Outline Plasmodium parasites and white blood cells.
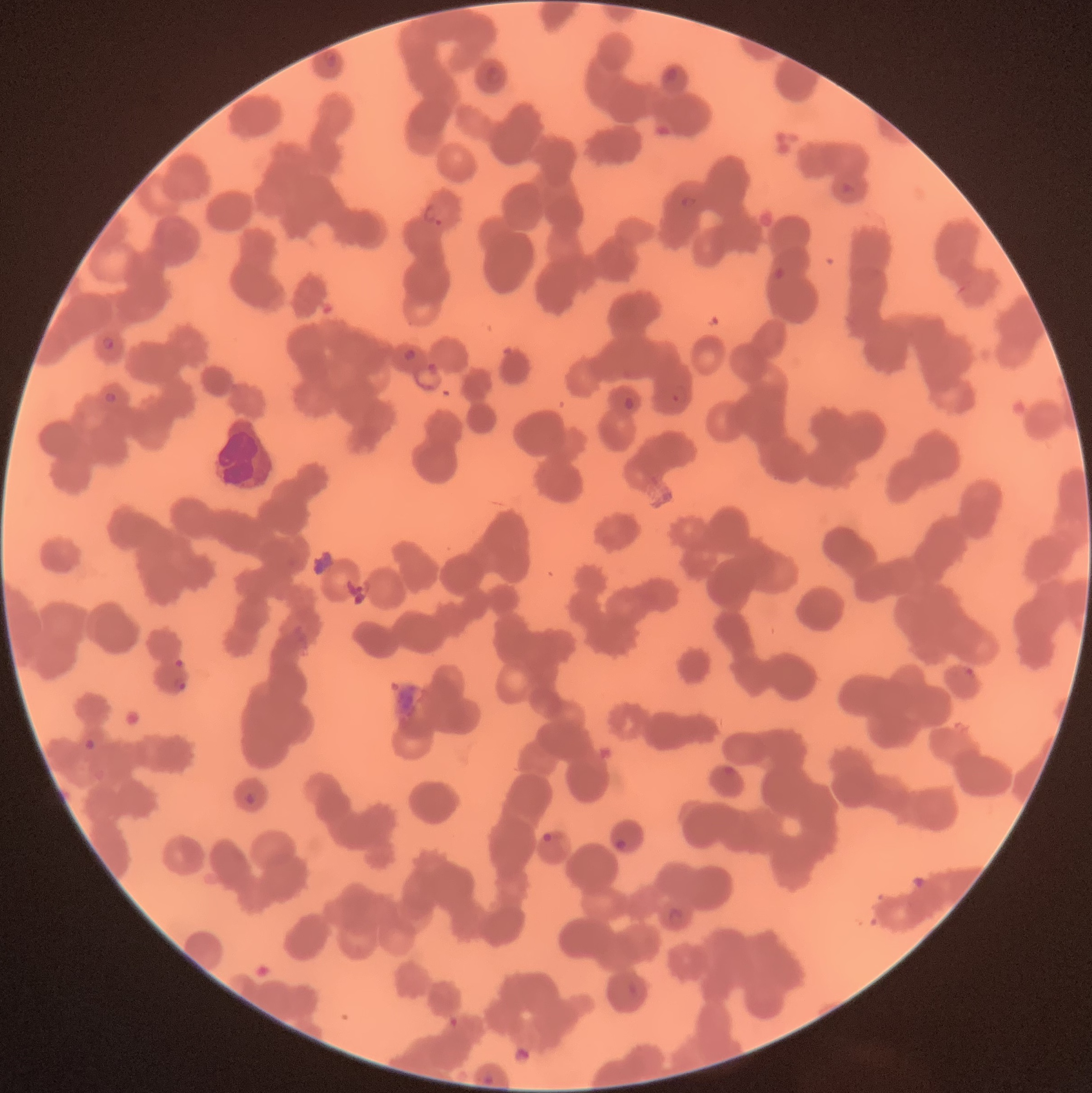

Approximate bounding boxes as [x1, y1, x2, y2] in pixels.
Plasmodium parasites: [323, 53, 337, 68], [484, 63, 503, 87], [664, 66, 680, 82], [839, 182, 857, 195], [680, 197, 697, 208], [423, 204, 444, 226], [100, 336, 117, 350], [669, 385, 690, 404], [104, 392, 117, 404], [175, 658, 184, 666], [964, 666, 976, 678], [168, 677, 186, 692], [83, 738, 95, 751], [245, 792, 257, 803], [543, 833, 565, 845], [612, 838, 627, 850], [669, 907, 684, 923], [630, 980, 647, 999].
White blood cells: [217, 418, 273, 487].

modality = light microscopy
image size = 1092×1093 pixels
red blood cell morphology = rouleaux formation
preparation = thin blood smear